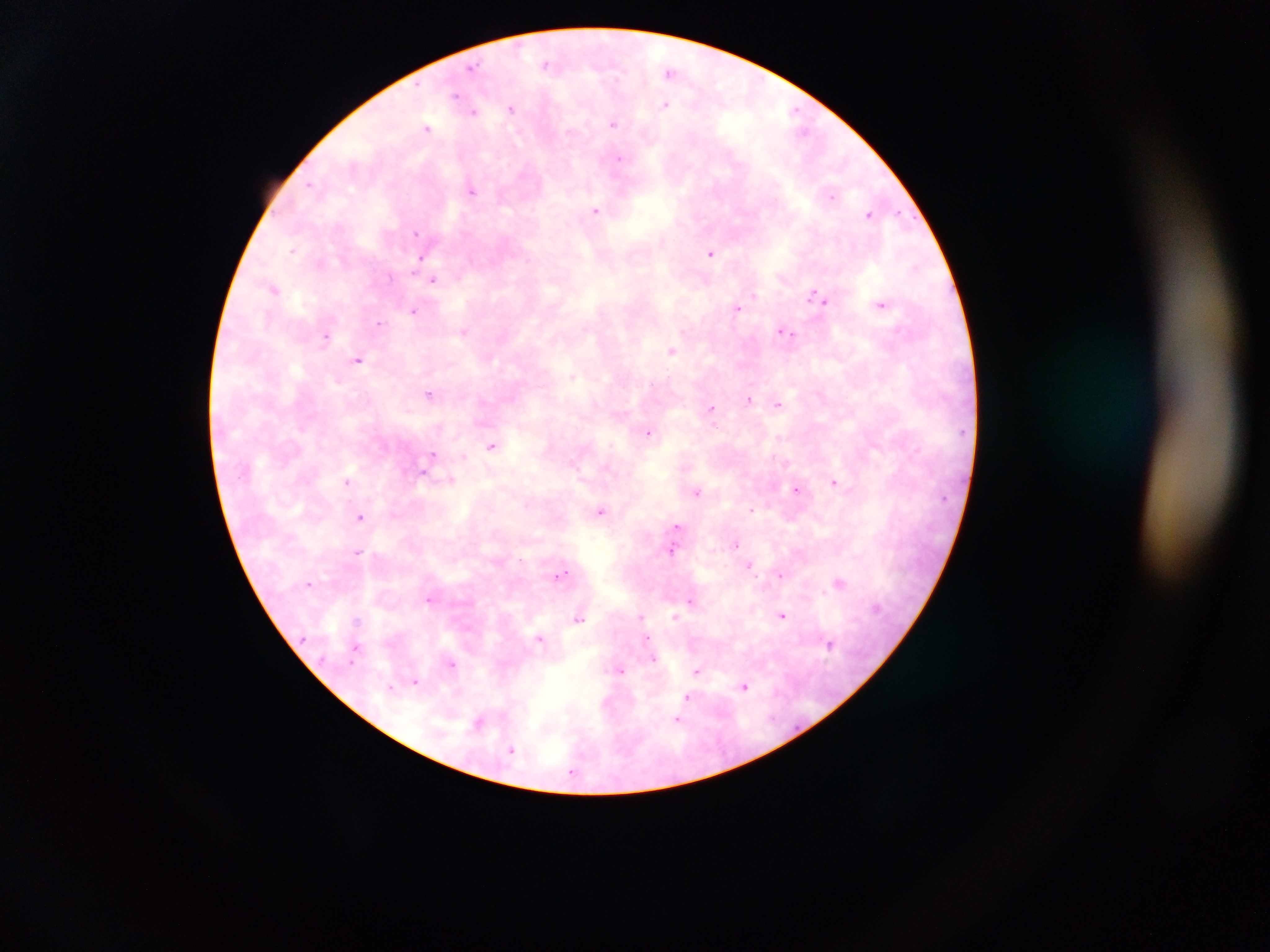

Approximate centers as [x, y] in pixels.
Summary:
  - Malaria parasite locations: [546, 64], [472, 67], [671, 71], [456, 96], [665, 104], [511, 107], [473, 113], [613, 124], [427, 128], [619, 162], [470, 191], [595, 210], [417, 231], [710, 253], [421, 258], [434, 279], [818, 299], [882, 305], [737, 309], [414, 311], [379, 323], [464, 330], [787, 333], [326, 337], [672, 351], [357, 359], [430, 395], [749, 400], [779, 404], [710, 410], [649, 434], [780, 438], [492, 446], [571, 464], [347, 482], [835, 482], [797, 489], [697, 492], [752, 511], [600, 512], [361, 518], [678, 526], [735, 544], [359, 550], [671, 552], [750, 566], [561, 575], [780, 576], [309, 581], [839, 582], [431, 599], [692, 600], [782, 613], [640, 616], [675, 616], [356, 619], [579, 619], [354, 622], [830, 643], [358, 647], [652, 655], [452, 665], [619, 668], [697, 671], [416, 683], [393, 686], [744, 687], [687, 697], [678, 718], [512, 750]
  - Capture: mobile-phone photograph through a microscope
  - Field of view: single
  - Preparation: thick blood smear
  - Country: Ghana
  - Image size: 1270×952 pixels